Assess the morphology of the red blood cells.
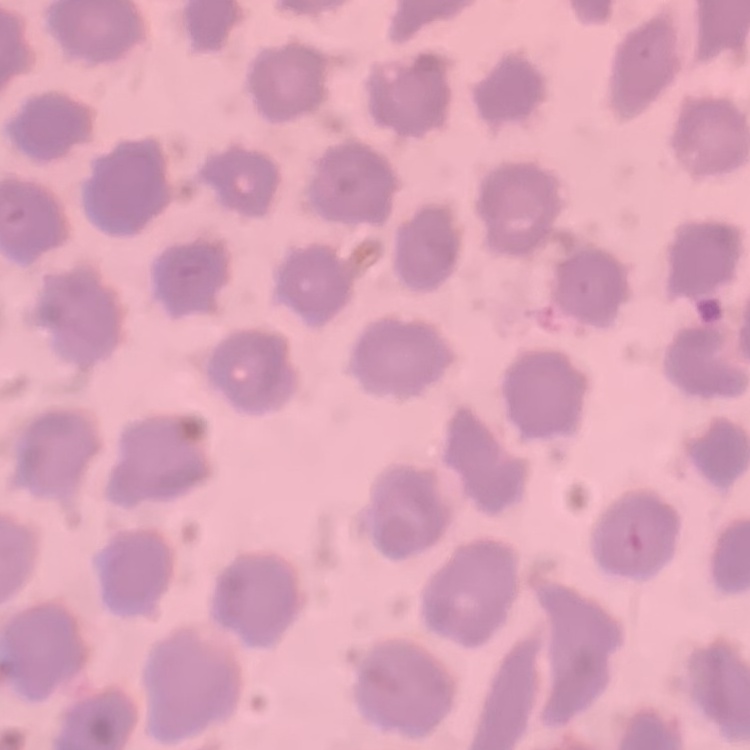

They show no rouleaux formation.

Summary:
  - Image type: square crop of a larger photomicrograph
  - Preparation: thin peripheral smear
  - Stain: Field's or Giemsa